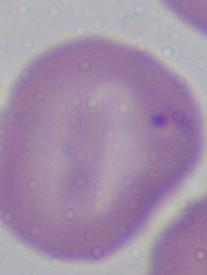
modality: photomicrograph
magnification: 1000x
identification: Babesia